Report the malaria status of this cell.
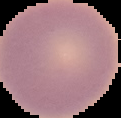

It is uninfected.

preparation = thin blood smear
image type = cell region segmented out of the field of view; surrounding area masked to black
image size = 121×118 pixels